Point out each Plasmodium parasite.
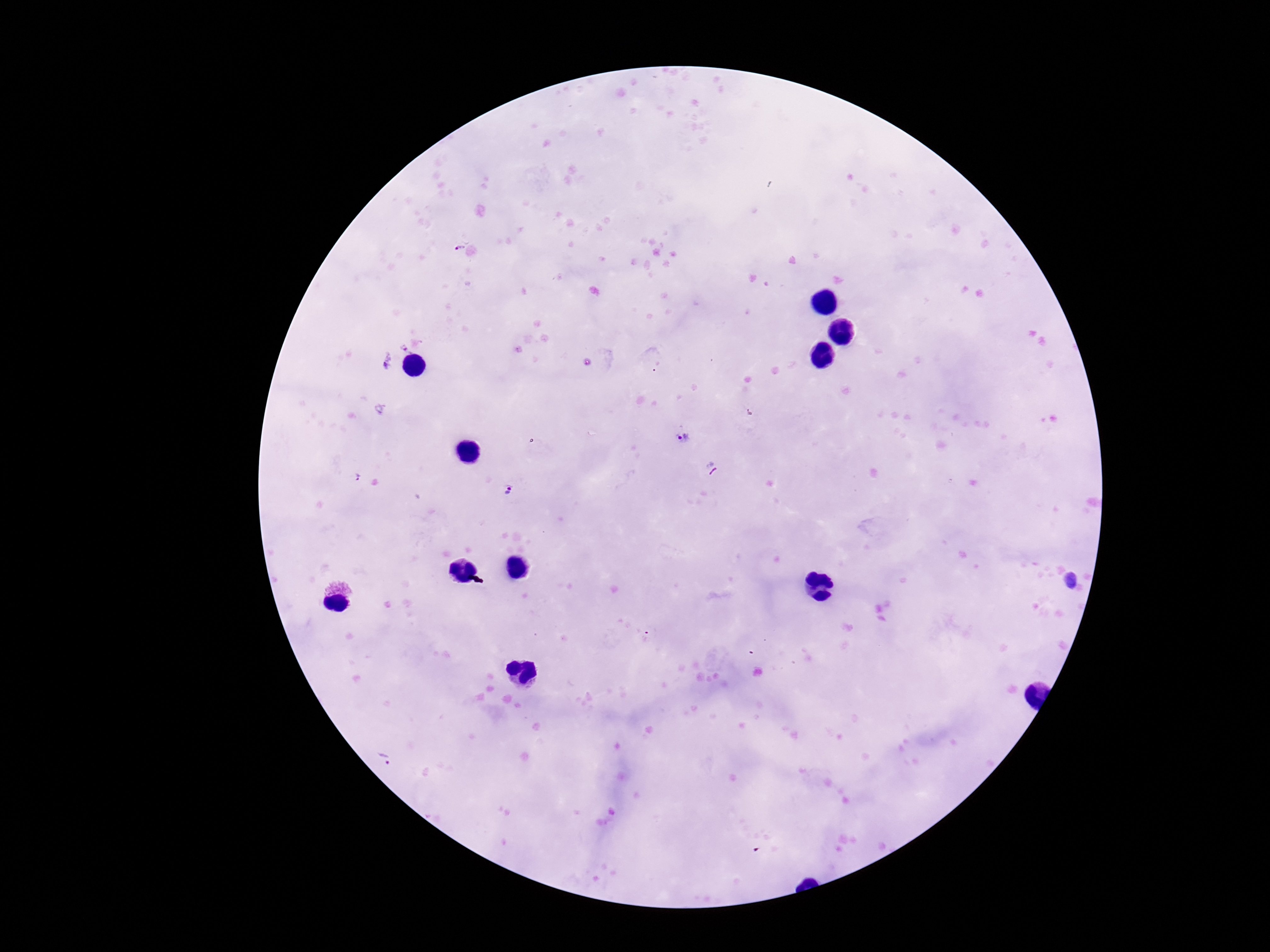
Approximate centers as [x, y] in pixels.
Plasmodium parasites: [459, 246], [683, 436], [359, 477], [513, 490], [1072, 580].

Giemsa stain. Thick blood smear. Patient malaria status: infected. 100x magnification. Photographed through the microscope eyepiece with a smartphone camera. Single field of view. Image is 1270×952 pixels.